Identify the blood parasite species.
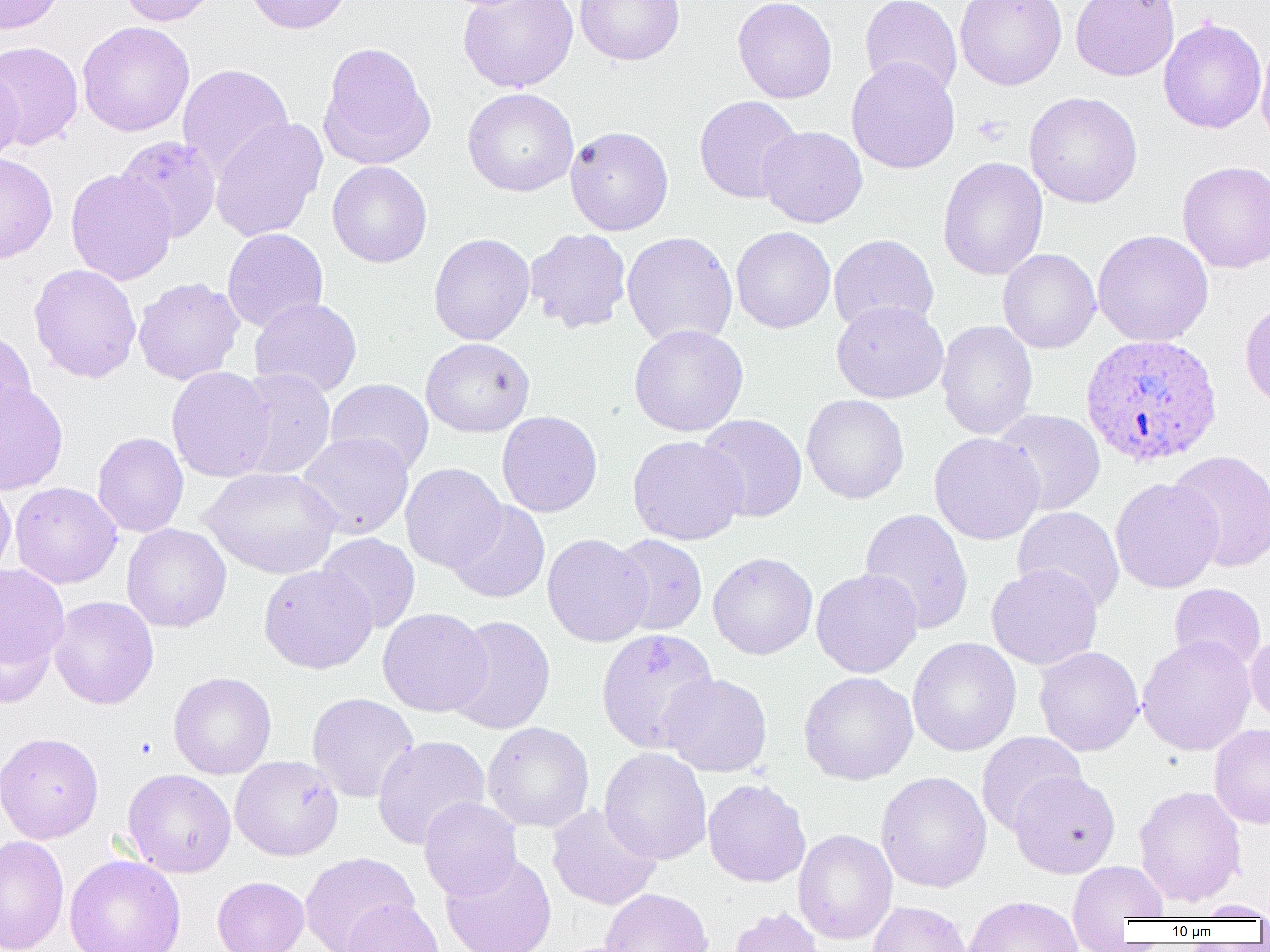
Plasmodium ovale.

modality = optical microscopy
Plasmodium ovale-infected red blood cell locations = approximate bounding boxes as [x1, y1, x2, y2] in pixels: [1080, 333, 1223, 467]
magnification = 1000x
preparation = thin blood film
field of view = single
platelet locations = approximate bounding boxes as [x1, y1, x2, y2] in pixels: [972, 113, 1011, 146], [643, 646, 675, 678]
image size = 1270×952 pixels
uninfected red blood cell locations = approximate bounding boxes as [x1, y1, x2, y2] in pixels: [0, 0, 64, 34], [118, 0, 220, 26], [243, 0, 353, 34], [458, 0, 578, 92], [575, 0, 684, 65], [733, 0, 837, 103], [860, 0, 962, 97], [956, 0, 1067, 90], [1071, 0, 1179, 81], [1159, 17, 1266, 134], [77, 21, 194, 137], [1255, 35, 1270, 151], [0, 40, 84, 151], [318, 41, 436, 170], [846, 58, 960, 174], [0, 64, 23, 164], [177, 64, 294, 178], [463, 87, 578, 197], [1024, 91, 1143, 208], [694, 95, 803, 204], [209, 117, 328, 242], [565, 125, 674, 235], [757, 126, 867, 227], [115, 135, 222, 242], [0, 152, 58, 264], [938, 156, 1048, 280], [1177, 160, 1270, 274], [327, 161, 432, 268], [65, 168, 177, 285], [731, 226, 836, 333], [222, 228, 328, 332], [525, 228, 631, 334], [1092, 229, 1214, 347], [622, 232, 738, 348], [428, 233, 535, 345], [829, 234, 939, 334], [998, 249, 1101, 353], [29, 263, 142, 384], [133, 277, 244, 385], [250, 297, 362, 398], [1240, 299, 1270, 412], [831, 300, 948, 403], [936, 320, 1038, 440], [629, 324, 749, 437], [0, 328, 36, 431], [421, 337, 535, 437], [166, 366, 277, 482], [232, 369, 336, 480], [326, 378, 433, 475], [0, 380, 68, 495], [801, 394, 909, 504], [991, 409, 1106, 515], [496, 411, 602, 517], [696, 414, 807, 522], [92, 432, 188, 537], [296, 432, 414, 539], [929, 432, 1045, 544], [627, 435, 747, 545], [1167, 450, 1270, 571], [400, 463, 506, 572], [200, 466, 341, 579], [0, 478, 16, 582], [1110, 478, 1224, 593], [10, 482, 122, 588], [447, 501, 550, 603], [1013, 506, 1125, 612], [859, 508, 974, 635], [122, 523, 231, 632], [317, 533, 420, 633], [542, 534, 653, 647], [609, 534, 708, 636], [708, 552, 818, 659], [0, 563, 70, 686], [986, 563, 1103, 670], [259, 564, 376, 673], [811, 568, 924, 678], [4, 579, 132, 696], [1169, 582, 1266, 672], [49, 596, 159, 709], [378, 607, 492, 717], [445, 615, 555, 735], [596, 629, 719, 756], [1246, 632, 1270, 727], [1137, 635, 1257, 756], [908, 637, 1021, 756], [1034, 646, 1144, 756], [168, 671, 277, 779], [799, 671, 919, 786], [660, 673, 772, 777], [306, 692, 419, 803], [482, 721, 595, 832], [1210, 724, 1270, 828], [0, 731, 104, 845], [977, 731, 1086, 834], [372, 735, 490, 849], [599, 747, 712, 865], [230, 755, 344, 861], [123, 769, 237, 878], [876, 771, 992, 893], [1010, 771, 1120, 878], [702, 778, 811, 887], [1133, 785, 1246, 907], [419, 797, 522, 901], [547, 804, 661, 910], [793, 829, 897, 945], [0, 834, 69, 952], [301, 852, 419, 952], [441, 853, 557, 952], [65, 855, 186, 952], [1068, 861, 1168, 935], [212, 876, 309, 952], [599, 888, 713, 952], [964, 895, 1083, 952], [341, 899, 443, 952], [1192, 900, 1270, 920], [867, 901, 972, 952], [728, 907, 826, 952]